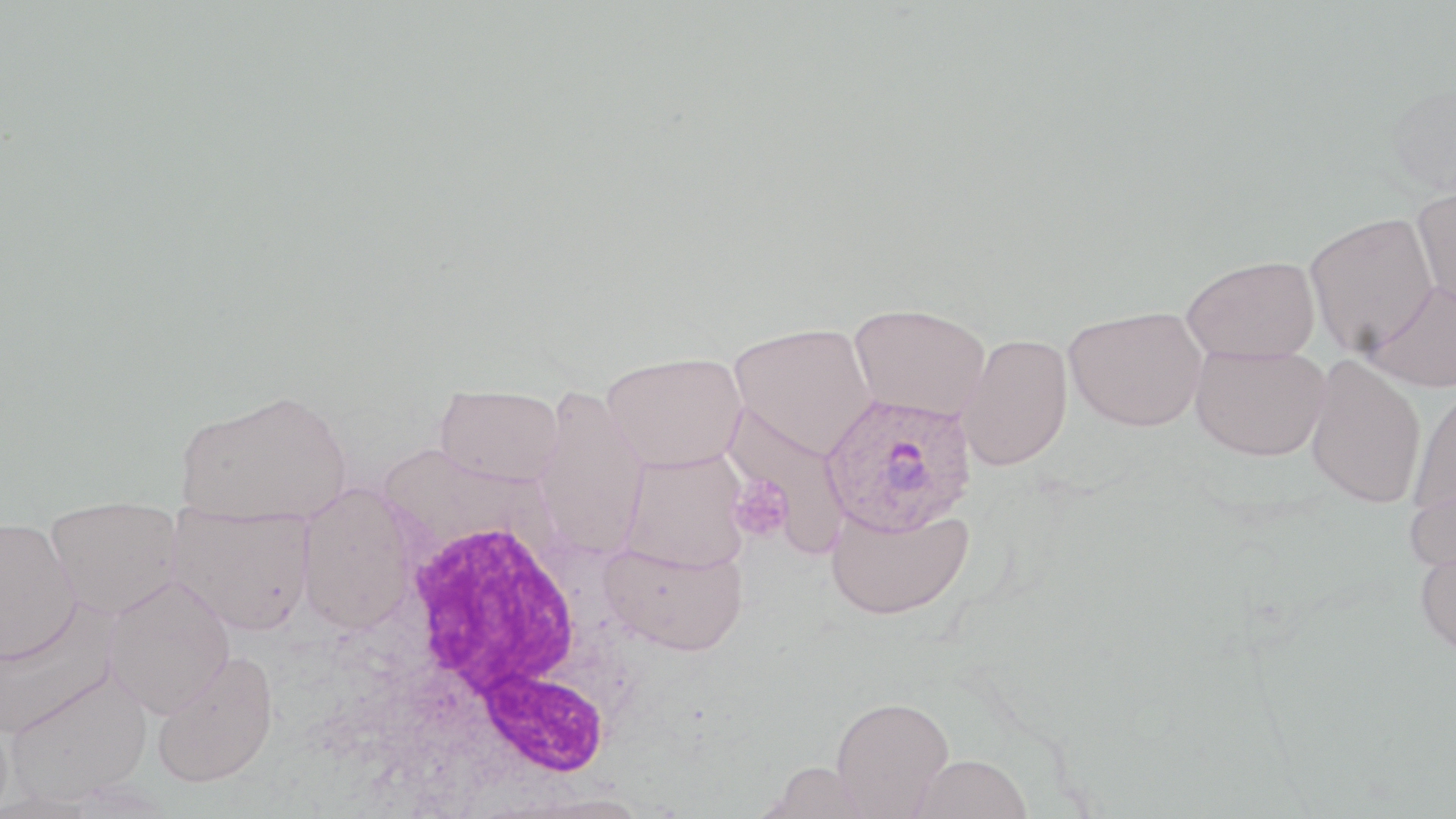
Approximate bounding boxes as (x1, y1, x2, y2) in pixels. Platelet locations: (727, 476, 795, 542). Plasmodium ovale-infected red blood cell locations: (820, 391, 978, 536). Uninfected red blood cell locations: (1384, 79, 1456, 204), (1411, 183, 1456, 313), (1303, 213, 1439, 355), (1181, 254, 1320, 362), (1363, 277, 1456, 392), (849, 303, 991, 423), (1065, 306, 1207, 431), (728, 322, 878, 459), (957, 333, 1073, 472), (1191, 344, 1330, 461), (601, 351, 748, 471), (1305, 356, 1427, 509), (435, 385, 565, 486), (533, 385, 650, 560), (1409, 385, 1456, 518), (174, 388, 351, 526), (726, 407, 853, 550), (618, 449, 750, 572), (1405, 476, 1456, 574), (296, 483, 417, 633), (43, 496, 187, 620), (825, 499, 975, 621), (167, 505, 315, 635), (0, 516, 82, 663), (599, 540, 749, 657), (1414, 540, 1456, 660), (103, 574, 235, 718), (0, 599, 120, 738), (151, 650, 280, 788), (4, 668, 153, 804), (831, 696, 954, 818), (909, 753, 1032, 818), (759, 761, 878, 818), (513, 794, 659, 819). White blood cell locations: (386, 509, 643, 785). Slide-level diagnosis: Plasmodium ovale. Thin blood film. Image is 1456×819 pixels. Optical microscopy. Single field of view. May-Grünwald-Giemsa-stained preparation. Captured at 1000x magnification.